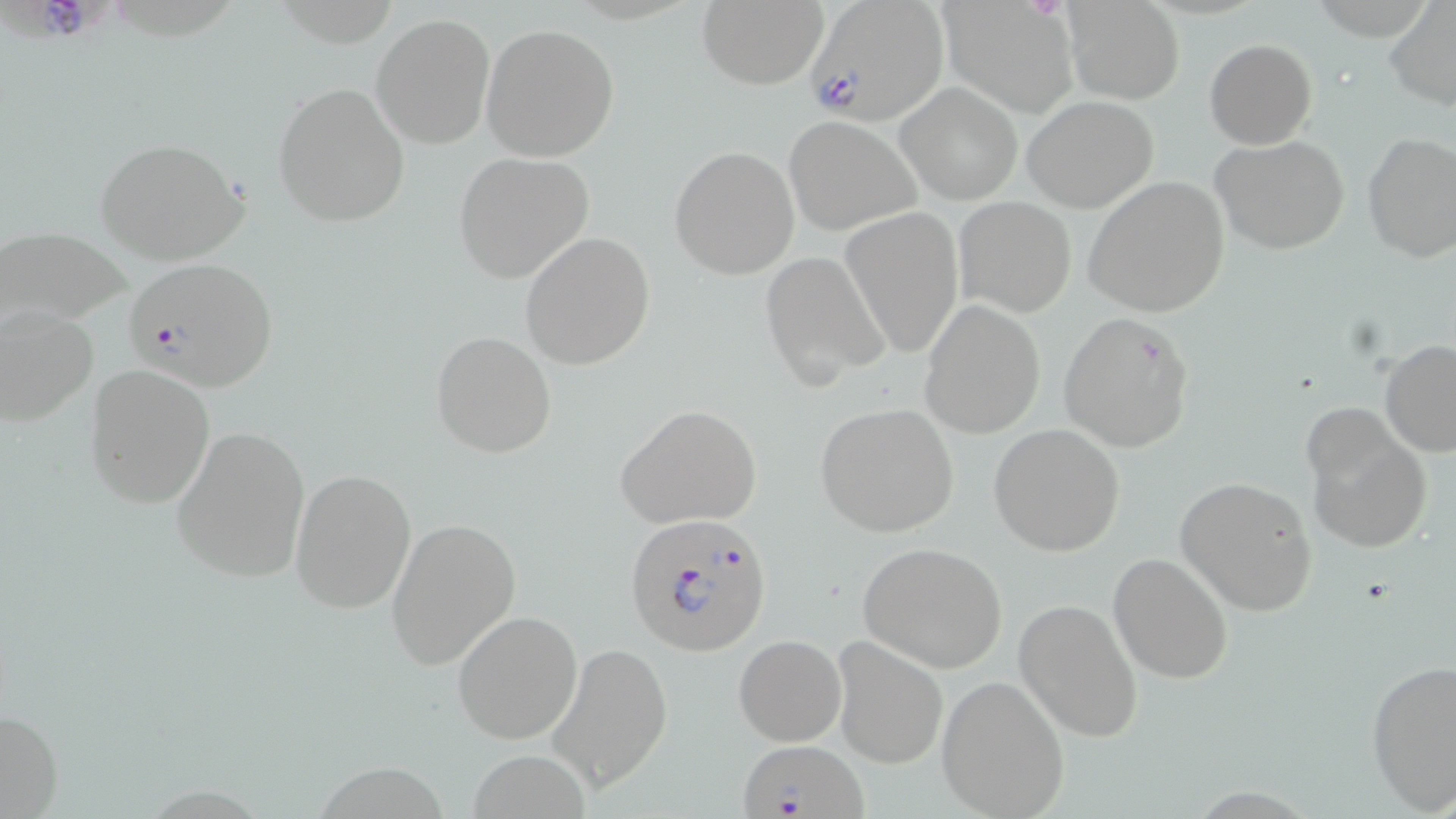

Approximate bounding boxes as (x1,y1)-(x2,y2) corner pairs in pixels. Uninfected red blood cell locations: (694,1)-(830,89), (1063,1)-(1185,105), (939,2)-(1077,116), (1382,3)-(1455,110), (371,13)-(495,149), (481,24)-(619,161), (1205,38)-(1316,148), (272,82)-(410,228), (896,82)-(1022,203), (1022,96)-(1160,211), (783,116)-(922,236), (1361,134)-(1456,263), (1211,135)-(1351,255), (95,136)-(250,266), (670,146)-(799,280), (454,152)-(595,286), (1083,176)-(1230,317), (954,197)-(1077,316), (839,208)-(964,360), (0,224)-(132,326), (520,232)-(655,370), (760,251)-(890,389), (920,300)-(1046,439), (1,304)-(98,428), (1058,313)-(1195,453), (430,330)-(557,458), (1380,340)-(1455,456), (85,363)-(216,509), (816,403)-(959,538), (614,404)-(762,529), (1303,405)-(1433,553), (170,424)-(310,586), (989,424)-(1126,556), (291,469)-(418,613), (1176,475)-(1319,615), (387,516)-(521,671), (858,543)-(1008,673), (1108,553)-(1233,683), (1013,598)-(1144,741), (452,611)-(582,744), (733,634)-(846,745), (829,635)-(949,769), (549,644)-(671,795), (1365,658)-(1456,812), (937,675)-(1070,816), (0,706)-(63,816). Plasmodium falciparum-infected red blood cell locations: (3,0)-(118,58), (805,0)-(946,123), (123,256)-(279,393), (622,511)-(775,655), (738,740)-(866,819). Slide-level diagnosis: Plasmodium falciparum. Image is 1456×819 pixels. Captured at 1000x magnification. One field of a larger specimen. Thin blood smear. May-Grünwald-Giemsa stain. Optical microscopy.